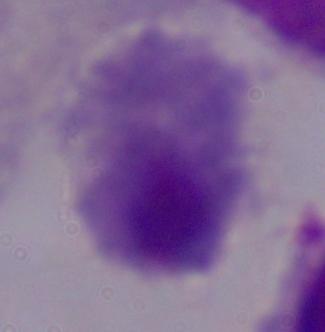 1000x magnification. Photomicrograph. A trichomonad is seen.